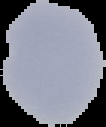

From a thin blood smear. Cell region segmented out of the field of view; the surrounding area is masked to black. Result: negative for malaria parasites. Image is 106×127 pixels.